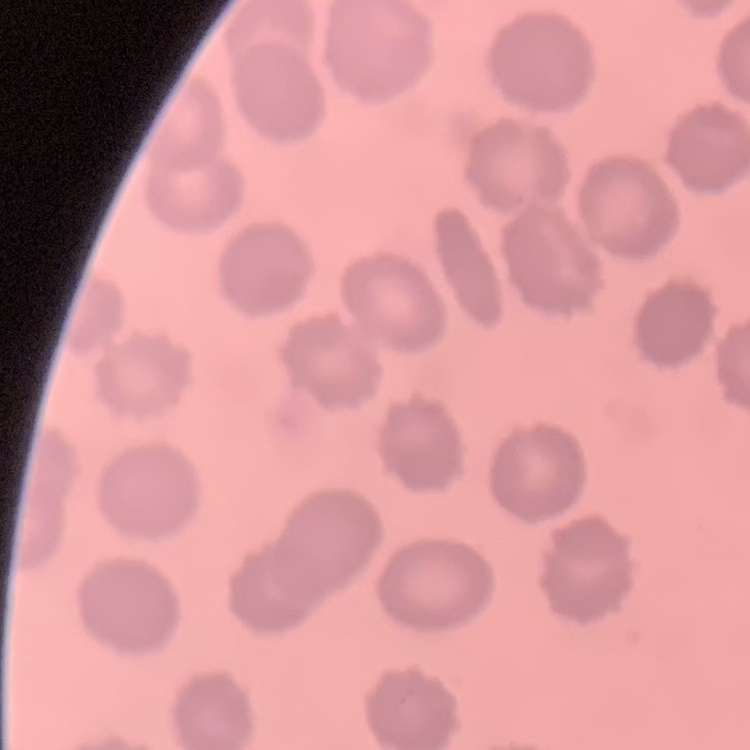

Summary:
  - Red blood cell morphology: no rouleaux formation
  - Image type: square crop of a larger photomicrograph
  - Stain: Field's or Giemsa
  - Preparation: thin blood smear